Identify the cell.
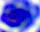
This is a leukocyte.

Micrograph. Captured at 400x magnification.